Outline each blood parasite and name the species.
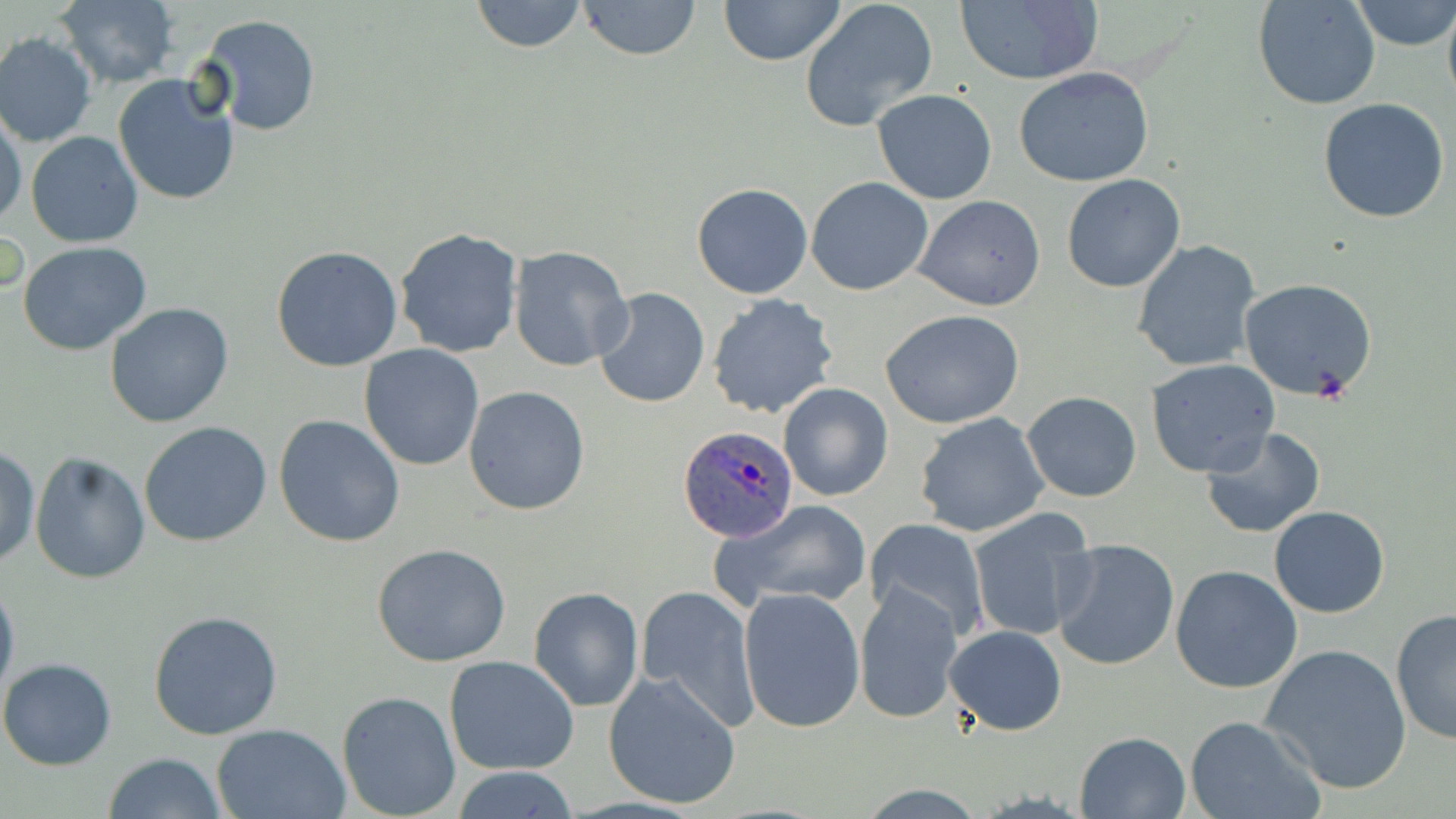

Approximate bounding boxes as (x1,y1)-(x2,y2) corner pairs in pixels.
Plasmodium ovale-infected red blood cells: (677,424)-(799,542).
No Plasmodium falciparum, Plasmodium malariae, Plasmodium vivax, Babesia divergens, or Trypanosoma brucei observed.

Uninfected red blood cell locations: (467,0)-(591,53), (574,0)-(705,61), (718,0)-(846,66), (798,0)-(940,132), (1350,0)-(1455,50), (54,1)-(181,87), (953,1)-(1103,85), (1253,1)-(1382,110), (1443,4)-(1456,111), (196,14)-(322,135), (0,33)-(96,148), (1014,67)-(1154,187), (112,73)-(241,206), (870,89)-(998,205), (1318,97)-(1452,223), (0,108)-(27,231), (26,131)-(143,247), (1061,173)-(1187,292), (806,176)-(934,296), (691,182)-(814,300), (913,195)-(1046,312), (395,227)-(524,358), (1132,240)-(1260,373), (17,241)-(152,354), (272,245)-(403,371), (508,245)-(632,372), (1239,279)-(1379,402), (592,287)-(709,408), (706,293)-(841,421), (105,301)-(234,429), (880,308)-(1025,428), (358,345)-(485,470), (1147,359)-(1280,478), (777,382)-(893,502), (463,385)-(592,515), (1021,391)-(1142,502), (913,412)-(1051,538), (274,413)-(406,547), (138,421)-(272,547), (1200,426)-(1327,539), (0,443)-(40,570), (30,453)-(150,584), (711,499)-(875,613), (1269,505)-(1392,618), (967,514)-(1097,643), (865,517)-(989,641), (1051,539)-(1179,671), (372,544)-(513,667), (1169,565)-(1302,694), (0,575)-(19,709), (635,584)-(760,731), (853,584)-(964,726), (529,586)-(644,712), (737,586)-(866,733), (1391,607)-(1456,746), (148,609)-(283,741), (945,624)-(1067,736), (1261,643)-(1411,794), (443,654)-(580,775), (0,657)-(116,770), (604,672)-(741,809), (337,690)-(461,819), (1185,716)-(1321,819), (213,722)-(350,818), (1075,730)-(1192,819), (104,752)-(227,819), (449,767)-(583,819). Slide-level diagnosis: Plasmodium ovale. Light microscopy. Captured at 1000x magnification. Thin blood film. One field of a larger specimen. May-Grünwald-Giemsa-stained preparation. Image is 1456×819 pixels.